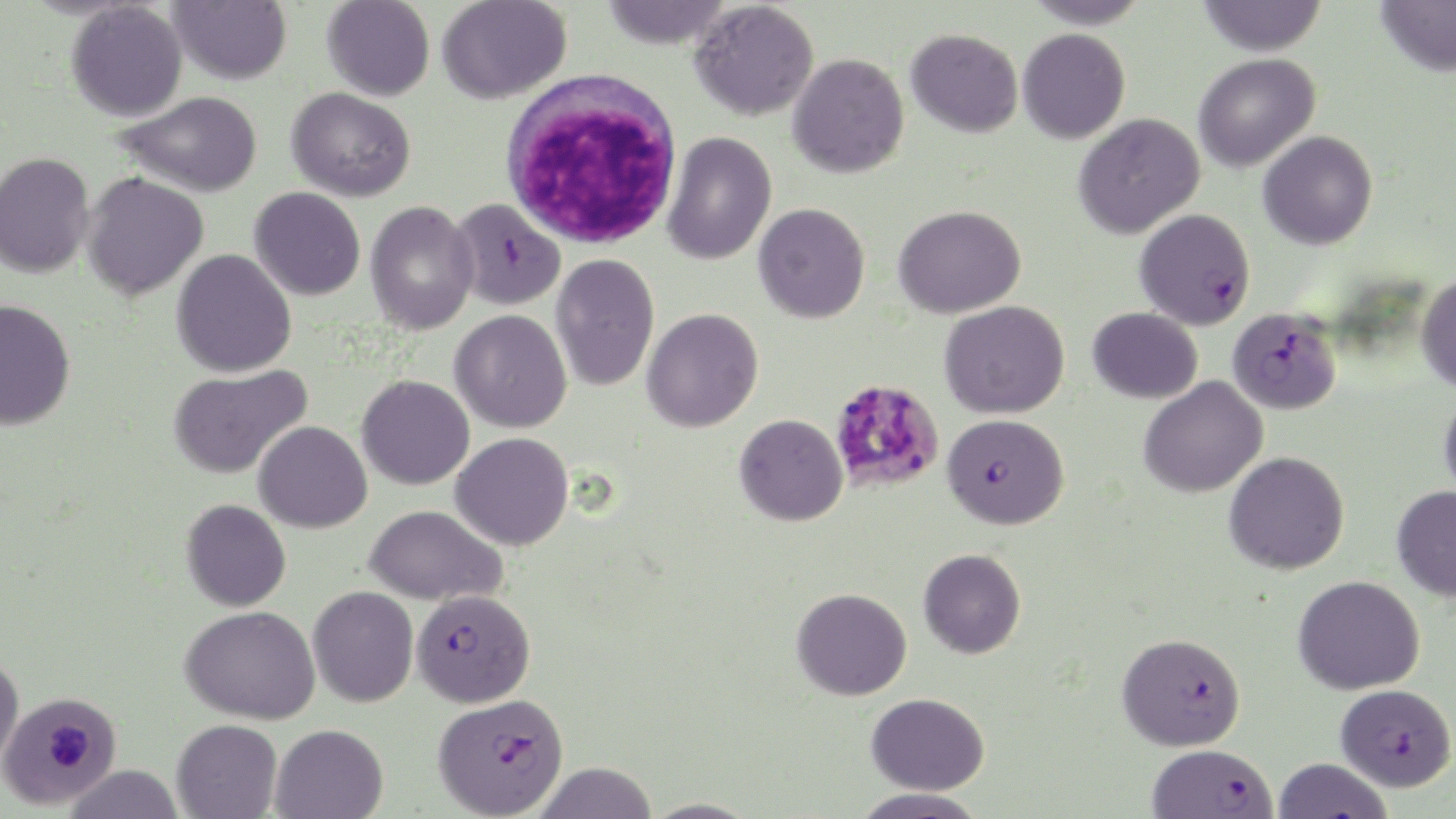
Summary:
  - Coordinate format: approximate bounding boxes as (x1,y1)-(x2,y2) corner pairs in pixels
  - Plasmodium falciparum-infected red blood cell locations: (451,197)-(565,311), (1135,208)-(1256,329), (1227,307)-(1342,415), (942,413)-(1069,529), (412,589)-(536,708), (1117,632)-(1246,750), (1335,683)-(1456,791), (0,689)-(122,809), (432,692)-(569,818), (1148,743)-(1277,818), (1272,757)-(1393,819)
  - White blood cell locations: (500,70)-(684,249)
  - Uninfected red blood cell locations: (168,0)-(292,85), (322,0)-(435,101), (437,0)-(571,104), (598,0)-(733,50), (1023,0)-(1153,29), (1197,0)-(1327,56), (1376,0)-(1456,76), (689,1)-(819,121), (66,2)-(188,122), (907,28)-(1023,137), (1018,28)-(1130,143), (787,53)-(910,178), (1193,53)-(1321,172), (287,87)-(416,201), (117,91)-(263,197), (1074,113)-(1205,239), (662,131)-(777,265), (1258,131)-(1378,250), (0,152)-(95,278), (81,172)-(209,301), (249,187)-(366,301), (365,202)-(479,336), (753,203)-(870,323), (893,205)-(1026,318), (171,249)-(297,378), (550,254)-(659,391), (1415,275)-(1456,392), (0,299)-(76,430), (940,300)-(1070,418), (1088,307)-(1203,403), (642,308)-(764,432), (449,309)-(572,432), (167,364)-(312,479), (357,375)-(475,490), (1139,376)-(1268,498), (1439,390)-(1456,501), (734,414)-(847,526), (253,420)-(373,533), (450,432)-(574,551), (1224,451)-(1350,575), (1392,486)-(1456,600), (181,499)-(291,611), (365,505)-(507,606), (918,548)-(1026,659), (1293,575)-(1425,695), (308,586)-(418,707), (791,587)-(912,700), (181,605)-(320,724), (0,651)-(24,770), (866,693)-(990,795), (172,719)-(282,819), (271,723)-(388,818), (532,762)-(658,819), (64,764)-(184,819), (853,787)-(988,818), (643,797)-(760,818)
  - Slide-level diagnosis: Plasmodium falciparum
  - Field of view: single
  - Magnification: 1000x
  - Stain: May-Grünwald-Giemsa
  - Image size: 1456×819 pixels
  - Preparation: thin blood film
  - Modality: optical microscopy